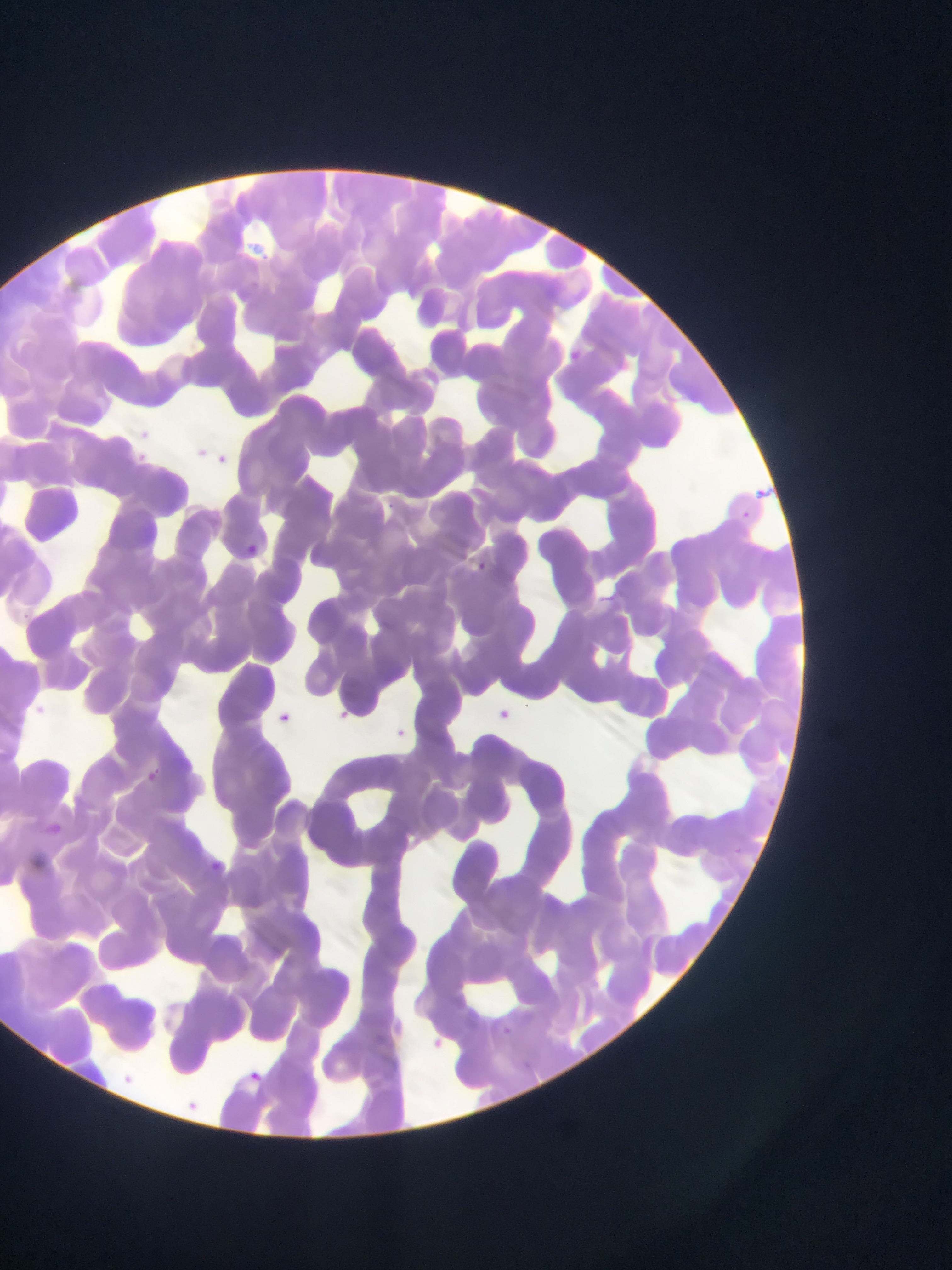
preparation = thin blood smear
image size = 952×1270 pixels
field of view = single
country = Ghana
capture = mobile-phone photograph through a microscope
Plasmodium parasite locations = approximate bounding boxes as (left, top, right, bottom) in pixels: (569, 347, 583, 363), (140, 430, 151, 441), (196, 448, 211, 459), (137, 452, 149, 462), (216, 453, 227, 462), (384, 500, 395, 509), (742, 510, 750, 519), (245, 542, 260, 557), (476, 560, 488, 570), (19, 611, 32, 622), (498, 707, 513, 723), (277, 710, 291, 724), (340, 710, 350, 719), (397, 728, 409, 739), (147, 770, 158, 782), (766, 798, 780, 808), (51, 822, 62, 834), (732, 845, 747, 855), (211, 860, 225, 875), (502, 1024, 514, 1036), (432, 1035, 445, 1047), (520, 1056, 534, 1068), (248, 1070, 260, 1083)